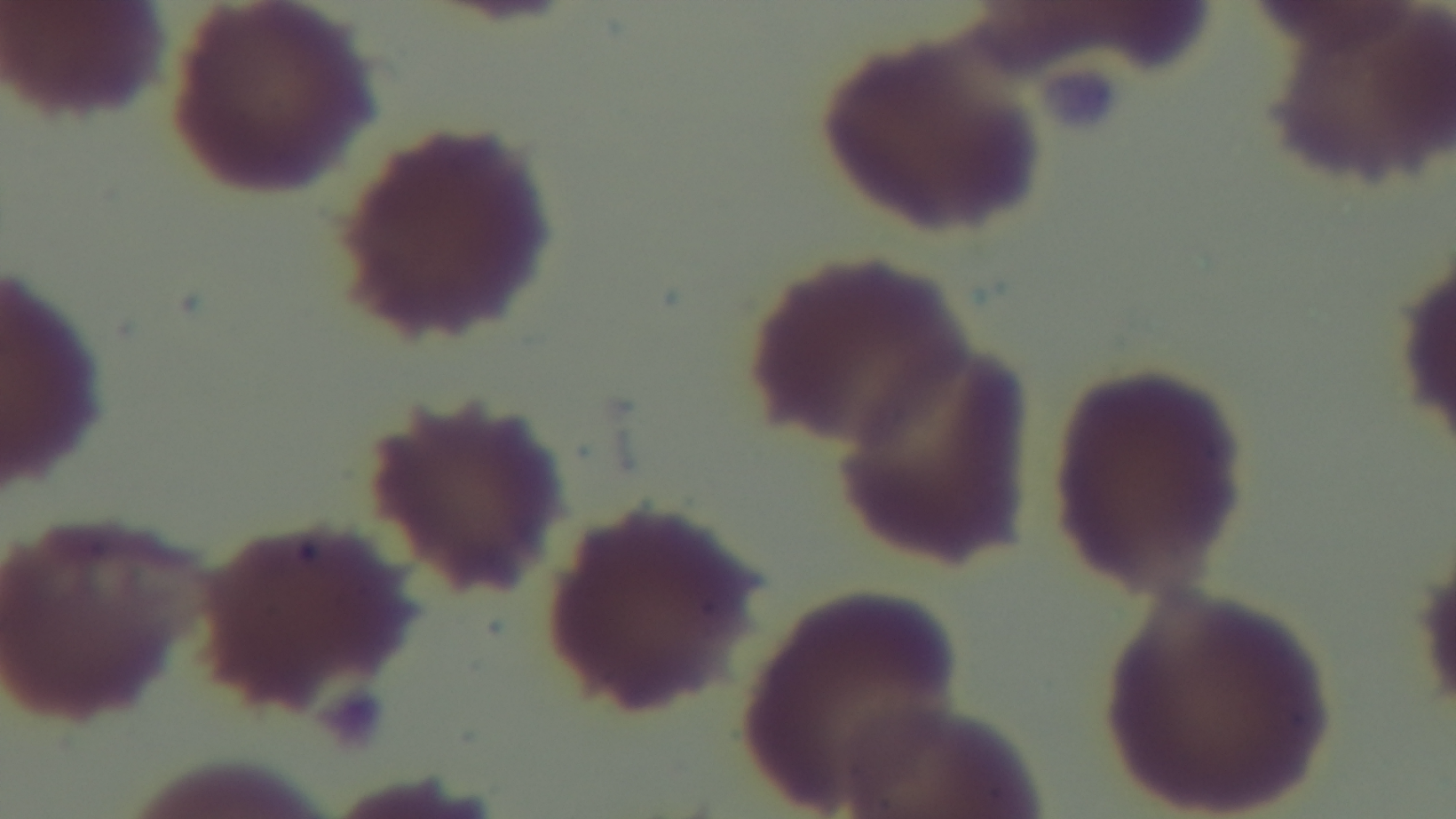

{
  "malaria_status": "uninfected",
  "objective": "100x oil immersion",
  "field_of_view": "one from the slide",
  "stain": "Giemsa",
  "capture": "mounted 4K digital camera",
  "preparation": "thin blood film",
  "modality": "light microscopy"
}